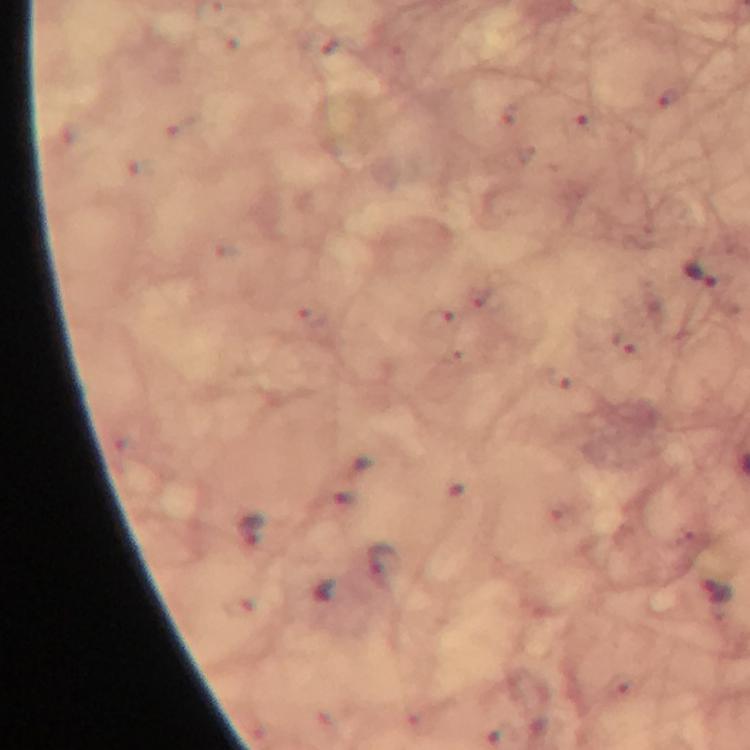
Approximate centers as (x, y) in pixels. Plasmodium parasite locations: (703, 279). From a diagnostic examination for malaria. Immersion oil applied. A crop from one field of view. Image is 750×750 pixels. Giemsa-stained preparation. Thick smear. 100x magnification. Photographed with a smartphone mounted on the microscope.